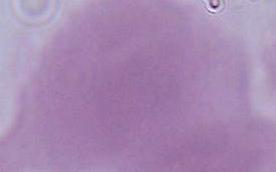
{
  "magnification": "1000x",
  "modality": "micrograph",
  "identification": "red blood cell"
}